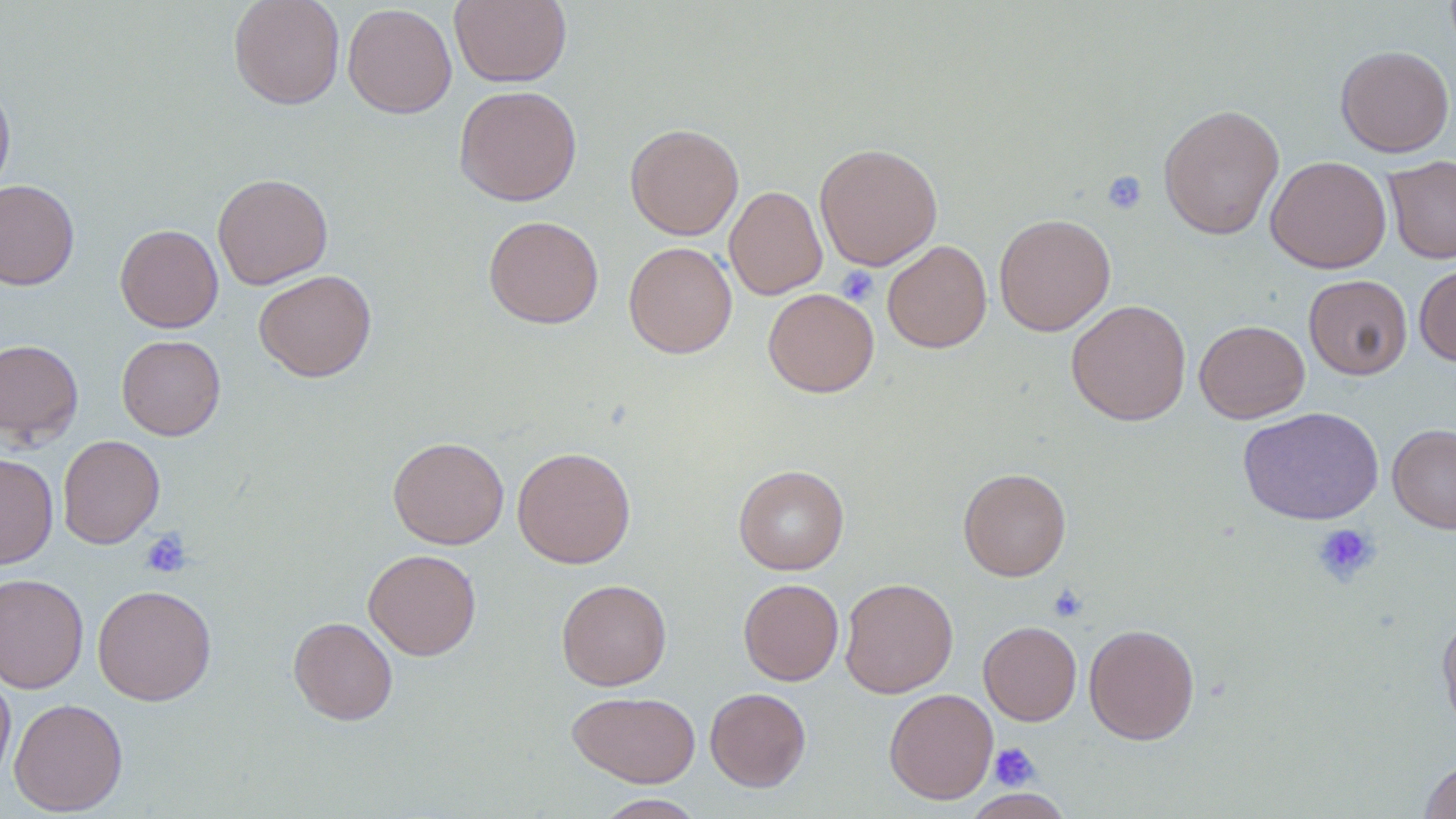

slide-level diagnosis = negative for blood parasites
preparation = thin blood film
platelet locations = approximate bounding boxes as [x1, y1, x2, y2] in pixels: [1101, 170, 1148, 215], [836, 265, 878, 306], [1312, 523, 1380, 586], [139, 528, 192, 579], [1048, 583, 1088, 622], [990, 742, 1041, 791]
field of view = single
magnification = 1000x
uninfected red blood cell locations = approximate bounding boxes as [x1, y1, x2, y2] in pixels: [228, 0, 346, 109], [449, 0, 572, 88], [342, 3, 457, 118], [1335, 45, 1455, 157], [0, 76, 15, 200], [453, 85, 582, 206], [1158, 104, 1285, 239], [625, 122, 744, 240], [814, 143, 943, 270], [1265, 155, 1391, 274], [1384, 155, 1456, 264], [212, 173, 333, 289], [0, 179, 80, 291], [725, 185, 827, 300], [994, 213, 1115, 335], [483, 215, 604, 329], [115, 224, 223, 333], [882, 240, 992, 352], [623, 241, 737, 359], [1414, 263, 1456, 366], [253, 269, 377, 382], [1303, 274, 1413, 380], [763, 287, 879, 398], [1066, 299, 1192, 425], [1194, 319, 1310, 423], [116, 334, 226, 440], [0, 338, 84, 446], [1237, 406, 1385, 525], [1387, 423, 1456, 534], [57, 434, 165, 549], [387, 436, 509, 549], [512, 446, 635, 568], [0, 452, 58, 569], [733, 464, 849, 574], [958, 467, 1071, 581], [363, 548, 481, 660], [0, 572, 89, 694], [839, 577, 959, 698], [556, 578, 671, 690], [739, 579, 844, 686], [92, 584, 217, 706], [1437, 611, 1456, 736], [288, 617, 398, 725], [978, 620, 1082, 726], [1083, 624, 1200, 745], [0, 668, 15, 791], [705, 687, 811, 791], [884, 688, 998, 804], [567, 691, 701, 788], [8, 697, 128, 816], [1419, 757, 1456, 818], [961, 789, 1076, 818], [593, 794, 707, 818]
stain = May-Grünwald-Giemsa
modality = light microscopy
image size = 1456×819 pixels